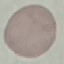
malaria status = uninfected
preparation = thin blood film
capture = smartphone through the microscope eyepiece
image type = cell patch, automatically extracted from a larger field of view and resized to 64 × 64 pixels
stain = Giemsa